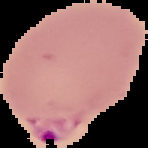

result = malaria parasites detected
image size = 148×148 pixels
preparation = thin blood smear
image type = segmented cell region with the area outside set to black